Report the malaria status.
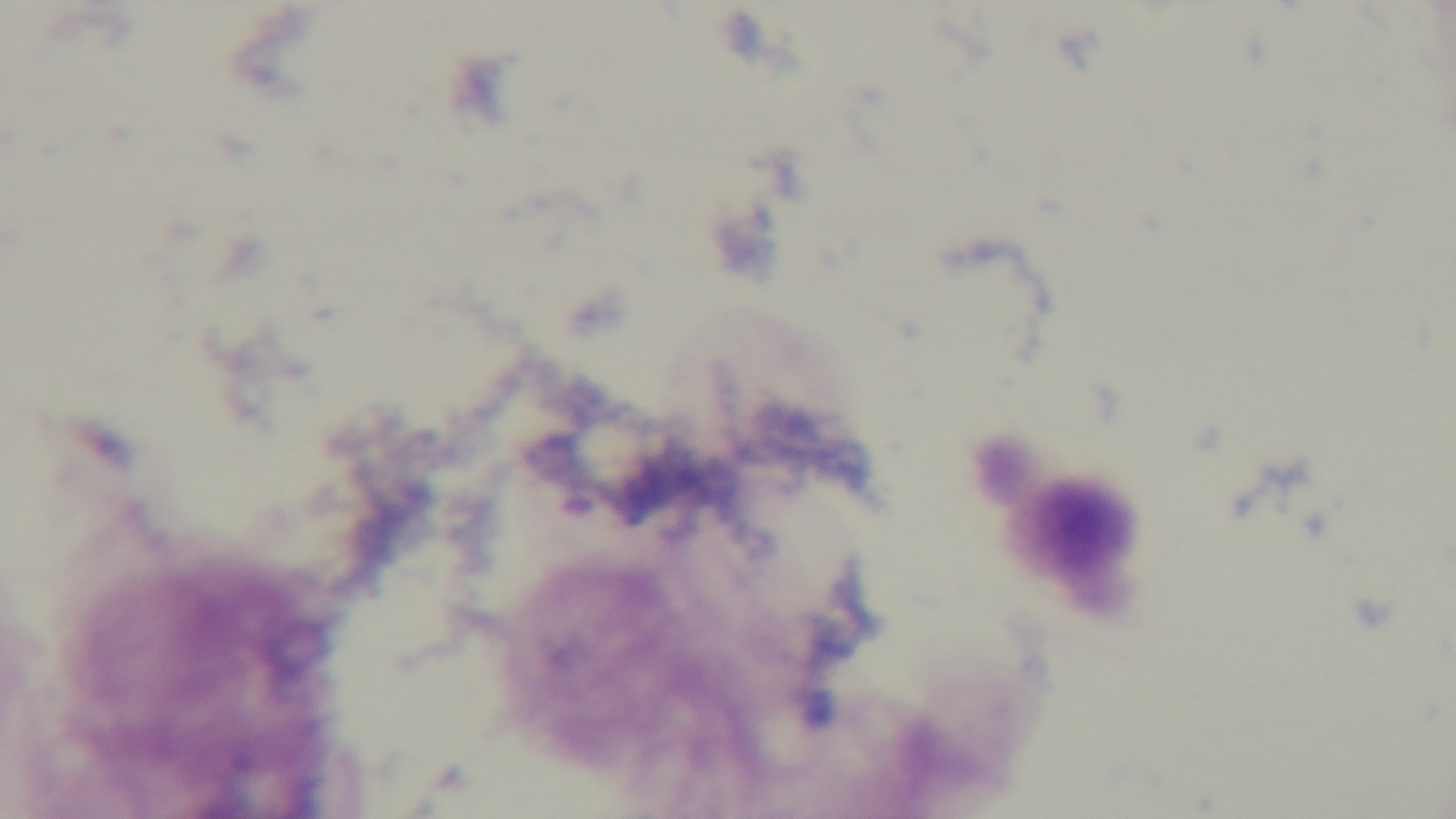

Negative.

Summary:
  - Capture: mounted 4K digital camera
  - Modality: light microscopy
  - Field of view: single
  - Objective: 100x oil immersion
  - Preparation: thick smear
  - Stain: Giemsa